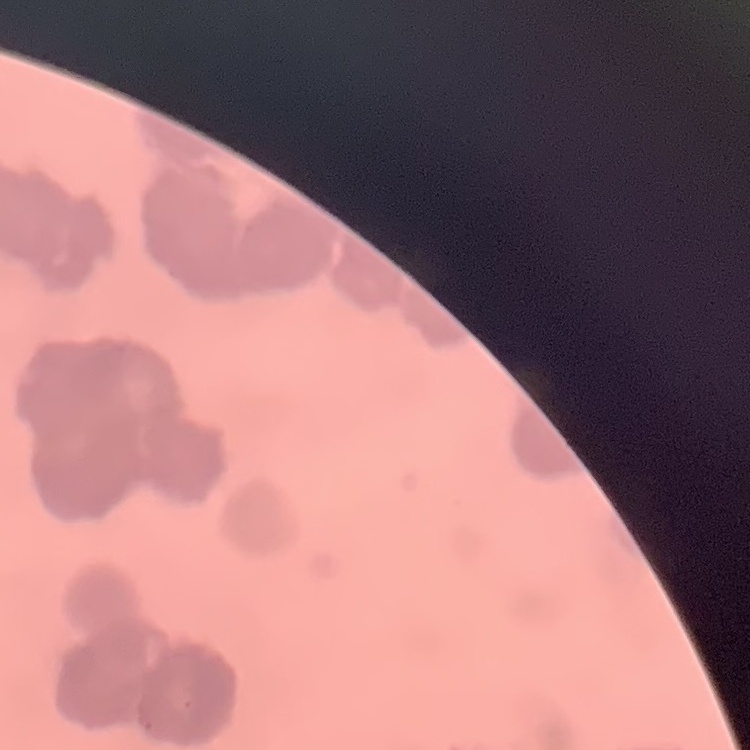
red blood cell morphology = rouleaux formation
preparation = thin blood smear
image type = square crop of a larger photomicrograph
stain = Field's or Giemsa